Assess this cell for malaria.
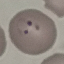

It is parasitized.

stain = Giemsa
preparation = thin blood smear
image type = automatically extracted cell patch, resized to 64 × 64 pixels
capture = smartphone through the microscope eyepiece